Report the malaria status of this cell.
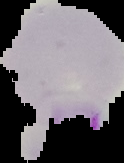

Parasitized.

Summary:
  - Image size: 124×163 pixels
  - Preparation: thin blood film
  - Image type: segmented cell region on a black background